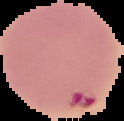

Summary:
  - Image type: cell region segmented out of the field of view; surrounding area masked to black
  - Result: Plasmodium parasites identified
  - Image size: 124×121 pixels
  - Preparation: thin blood film